Locate and identify every blood parasite.
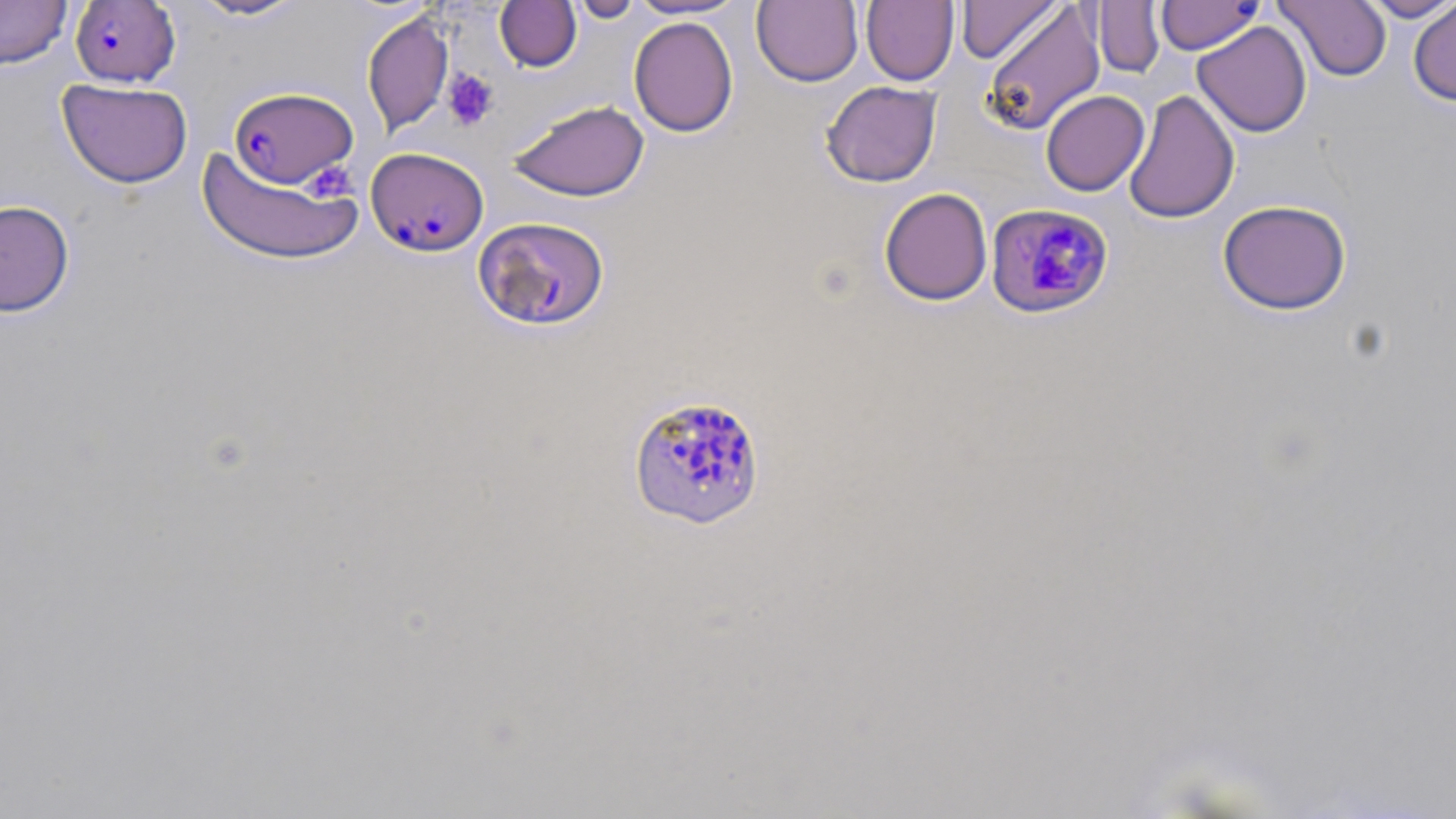
Approximate bounding boxes as (x1, y1, x2, y2) in pixels.
Plasmodium falciparum-infected red blood cells: (69, 1, 181, 88), (228, 87, 358, 189), (366, 147, 489, 257), (985, 203, 1115, 320), (473, 216, 609, 331), (627, 393, 767, 531).
No Plasmodium ovale, Plasmodium malariae, Plasmodium vivax, Babesia divergens, or Trypanosoma brucei observed.

Platelet locations: (443, 68, 499, 131), (304, 161, 357, 202). Uninfected red blood cell locations: (0, 0, 72, 68), (187, 0, 308, 21), (568, 0, 644, 23), (628, 0, 747, 20), (752, 0, 863, 87), (861, 0, 960, 85), (956, 0, 1063, 64), (1156, 0, 1262, 55), (1274, 0, 1391, 82), (1359, 0, 1456, 22), (1408, 0, 1456, 106), (495, 1, 582, 73), (981, 2, 1105, 136), (1091, 2, 1165, 78), (361, 10, 453, 138), (628, 16, 738, 137), (1192, 21, 1312, 137), (56, 78, 194, 188), (820, 81, 942, 187), (1123, 89, 1240, 225), (1040, 90, 1149, 196), (507, 99, 650, 202), (197, 145, 363, 266), (878, 187, 993, 306), (0, 199, 75, 317), (1217, 199, 1352, 315). Slide-level diagnosis: Plasmodium falciparum. Image is 1456×819 pixels. 1000x magnification. Thin blood smear. May-Grünwald-Giemsa stain. One field of a larger specimen. Optical microscopy.